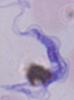
Summary:
  - Identification: trypanosome
  - Magnification: 1000x
  - Modality: micrograph